Classify this cell by malaria status.
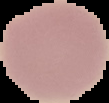

It is uninfected.

Summary:
  - Image size: 109×103 pixels
  - Preparation: thin blood film
  - Image type: segmented cell region on a black background